Locate every Plasmodium parasite and every leukocyte.
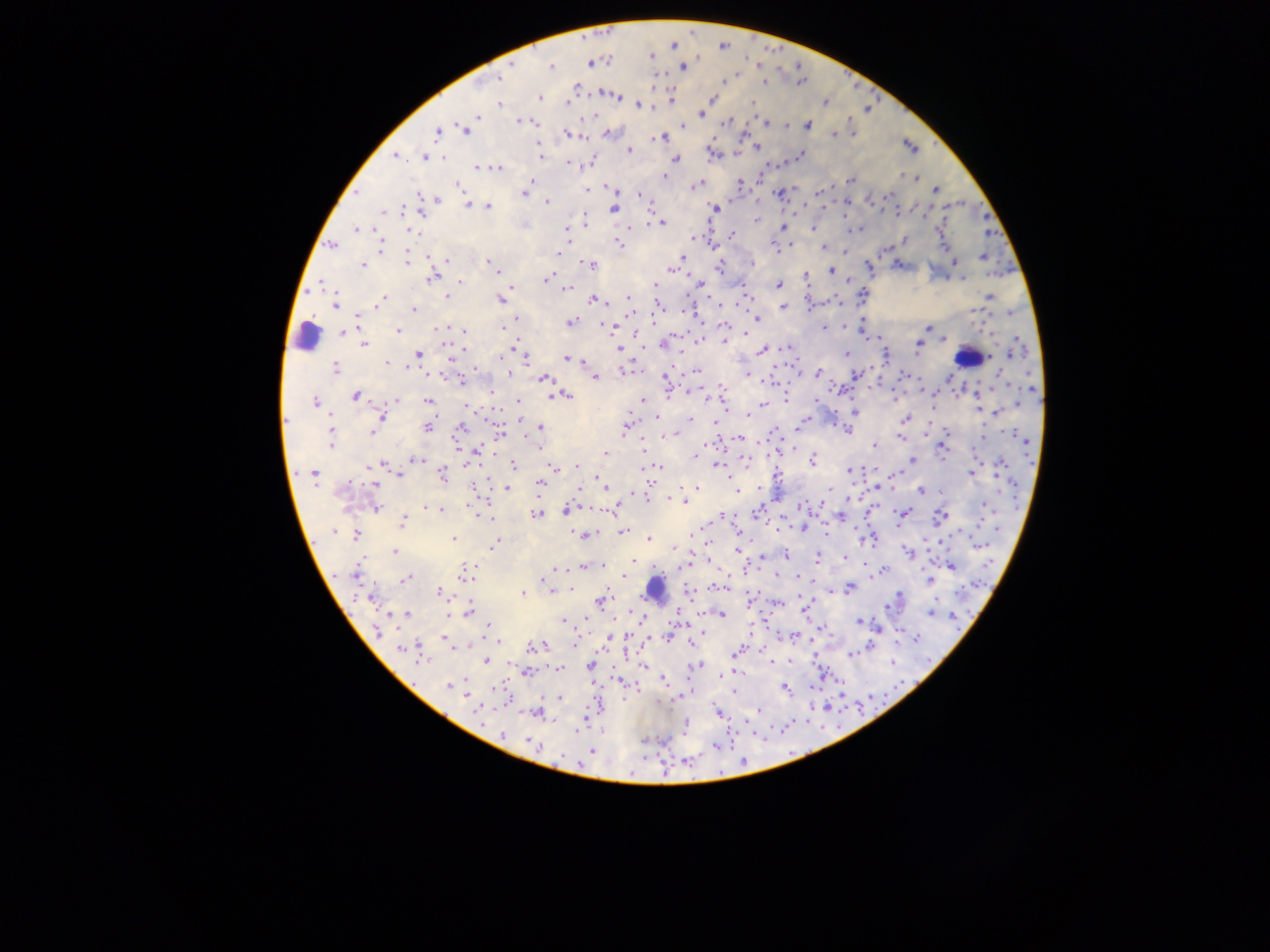
Approximate centers as [x, y] in pixels.
Plasmodium parasites: [752, 37], [673, 45], [723, 45], [769, 52], [651, 56], [590, 63], [512, 64], [758, 64], [798, 64], [551, 66], [683, 66], [845, 75], [497, 77], [724, 81], [798, 81], [764, 83], [855, 84], [575, 86], [872, 89], [602, 93], [615, 95], [539, 97], [671, 97], [710, 99], [567, 102], [824, 102], [751, 103], [499, 104], [639, 105], [864, 108], [703, 112], [701, 113], [591, 114], [476, 116], [850, 116], [518, 121], [725, 122], [764, 123], [786, 125], [683, 126], [806, 126], [464, 129], [437, 130], [566, 133], [607, 133], [743, 133], [853, 133], [834, 134], [661, 138], [757, 146], [910, 146], [629, 149], [735, 150], [712, 153], [800, 155], [395, 156], [541, 156], [424, 157], [675, 159], [591, 160], [785, 160], [567, 164], [479, 167], [495, 167], [760, 175], [901, 175], [663, 177], [915, 177], [531, 179], [851, 180], [739, 183], [698, 184], [458, 185], [527, 185], [586, 189], [611, 189], [780, 191], [934, 191], [820, 192], [890, 192], [523, 194], [638, 194], [435, 199], [869, 199], [962, 201], [545, 202], [844, 203], [466, 205], [802, 205], [916, 206], [488, 207], [614, 208], [824, 208], [715, 209], [944, 209], [403, 210], [385, 211], [421, 211], [898, 216], [987, 216], [756, 218], [585, 220], [648, 221], [662, 223], [566, 227], [781, 227], [814, 228], [860, 228], [356, 229], [936, 229], [408, 231], [988, 232], [733, 235], [693, 237], [903, 240], [618, 244], [332, 245], [712, 245], [790, 245], [949, 246], [773, 247], [380, 248], [823, 248], [886, 248], [843, 249], [559, 252], [981, 256], [447, 258], [681, 259], [407, 260], [489, 262], [954, 262], [751, 263], [589, 264], [361, 265], [898, 265], [719, 267], [868, 267], [673, 269], [830, 270], [1007, 270], [495, 272], [431, 275], [804, 275], [688, 276], [546, 279], [847, 279], [946, 280], [459, 282], [699, 282], [654, 284], [778, 284], [512, 287], [566, 288], [686, 295], [862, 295], [504, 296], [988, 296], [447, 297], [746, 298], [382, 299], [629, 299], [500, 300], [593, 300], [741, 300], [712, 301], [605, 302], [838, 302], [335, 303], [654, 304], [811, 305], [782, 307], [414, 309], [680, 310], [973, 311], [1010, 312], [662, 314], [358, 316], [694, 316], [757, 319], [864, 320], [570, 323], [603, 325], [723, 326], [503, 327], [822, 327], [928, 327], [618, 328], [844, 328], [398, 330], [464, 331], [343, 332], [859, 332], [878, 338], [698, 339], [944, 339], [726, 340], [663, 343], [365, 344], [918, 345], [644, 347], [788, 347], [618, 348], [514, 349], [761, 349], [1012, 351], [418, 353], [845, 353], [885, 356], [451, 357], [525, 358], [565, 358], [583, 359], [385, 362], [334, 368], [408, 369], [624, 370], [696, 370], [510, 374], [818, 374], [856, 374], [904, 375], [747, 376], [950, 376], [999, 376], [594, 377], [543, 378], [799, 378], [665, 379], [772, 380], [461, 381], [721, 383], [879, 383], [1031, 388], [688, 392], [977, 392], [491, 393], [839, 393], [957, 394], [552, 395], [563, 395], [355, 396], [785, 397], [894, 398], [395, 399], [643, 400], [428, 401], [519, 401], [705, 401], [723, 401], [315, 402], [1039, 403], [763, 404], [818, 404], [1017, 404], [468, 407], [931, 407], [978, 408], [836, 412], [855, 413], [996, 413], [747, 415], [381, 416], [520, 419], [689, 419], [904, 419], [804, 420], [715, 424], [800, 425], [835, 425], [983, 425], [428, 426], [460, 427], [540, 427], [626, 427], [948, 427], [329, 429], [847, 430], [372, 431], [498, 431], [1009, 431], [330, 435], [665, 435], [922, 436], [900, 438], [739, 439], [1023, 440], [330, 444], [642, 444], [874, 445], [942, 446], [539, 447], [974, 448], [778, 450], [475, 452], [606, 454], [695, 455], [417, 458], [469, 458], [812, 459], [912, 460], [744, 463], [381, 464], [514, 465], [655, 465], [717, 465], [576, 466], [999, 466], [556, 467], [1031, 467], [864, 468], [848, 471], [972, 472], [312, 473], [400, 474], [441, 474], [896, 474], [996, 474], [598, 478], [650, 479], [778, 481], [539, 483], [376, 484], [854, 485], [604, 486], [732, 486], [696, 487], [876, 487], [1012, 487], [507, 488], [828, 488], [758, 489], [735, 490], [922, 490], [578, 491], [941, 492], [631, 495], [673, 497], [847, 499], [685, 502], [822, 502], [982, 505], [425, 506], [1017, 506], [376, 507], [801, 507], [441, 509], [567, 509], [612, 509], [993, 510], [758, 512], [867, 513], [902, 513], [536, 514], [721, 516], [782, 516], [940, 516], [840, 517], [490, 519], [826, 519], [401, 522], [976, 523], [792, 525], [805, 527], [896, 528], [776, 529], [998, 529], [854, 530], [337, 531], [623, 531], [354, 534], [582, 534], [827, 534], [691, 536], [873, 537], [453, 538], [649, 538], [941, 542], [493, 544], [978, 545], [876, 546], [672, 549], [737, 549], [393, 552], [908, 553], [925, 553], [786, 555], [761, 556], [844, 557], [817, 558], [632, 559], [711, 563], [864, 563], [601, 565], [685, 565], [582, 566], [950, 566], [554, 567], [882, 570], [466, 572], [988, 572], [356, 574], [623, 575], [796, 575], [775, 576], [870, 577], [405, 578], [930, 580], [812, 582], [962, 584], [548, 586], [714, 586], [719, 587], [849, 587], [568, 588], [551, 589], [832, 591], [440, 592], [688, 592], [522, 593], [901, 594], [370, 597], [600, 600], [749, 600], [778, 602], [805, 607], [888, 607], [468, 611], [679, 611], [720, 613], [930, 613], [952, 614], [405, 615], [690, 620], [765, 620], [563, 621], [860, 621], [641, 624], [487, 625], [822, 627], [959, 627], [878, 628], [378, 632], [627, 632], [898, 634], [793, 636], [650, 637], [666, 637], [917, 637], [444, 639], [608, 639], [691, 642], [541, 645], [575, 645], [870, 646], [468, 647], [403, 648], [415, 650], [738, 651], [853, 653], [735, 654], [624, 655], [852, 656], [815, 658], [790, 660], [486, 661], [771, 661], [893, 662], [700, 665], [590, 666], [643, 666], [558, 669], [735, 670], [526, 672], [823, 675], [663, 680], [619, 681], [449, 685], [498, 687], [896, 687], [464, 688], [784, 688], [636, 690], [734, 692], [682, 694], [841, 694], [678, 696], [868, 696], [560, 697], [622, 700], [602, 702], [823, 707], [857, 707], [757, 709], [536, 712], [717, 713], [480, 714], [583, 717], [807, 720], [685, 726], [784, 727], [821, 728], [740, 733], [502, 734], [642, 738], [662, 741], [533, 744], [716, 745], [592, 751], [790, 752], [686, 757], [645, 758], [742, 758], [664, 772].
Leukocytes: [307, 337], [967, 357], [654, 588].

{
  "image_size": "1270×952 pixels",
  "preparation": "thick blood film",
  "field_of_view": "single",
  "country": "Ghana",
  "capture": "mobile-phone photograph through a microscope"
}